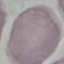

Summary:
  - Malaria status: uninfected
  - Image type: automatically extracted cell patch, resized to 64 × 64 pixels
  - Preparation: thin blood smear
  - Stain: Giemsa
  - Capture: smartphone through the microscope eyepiece